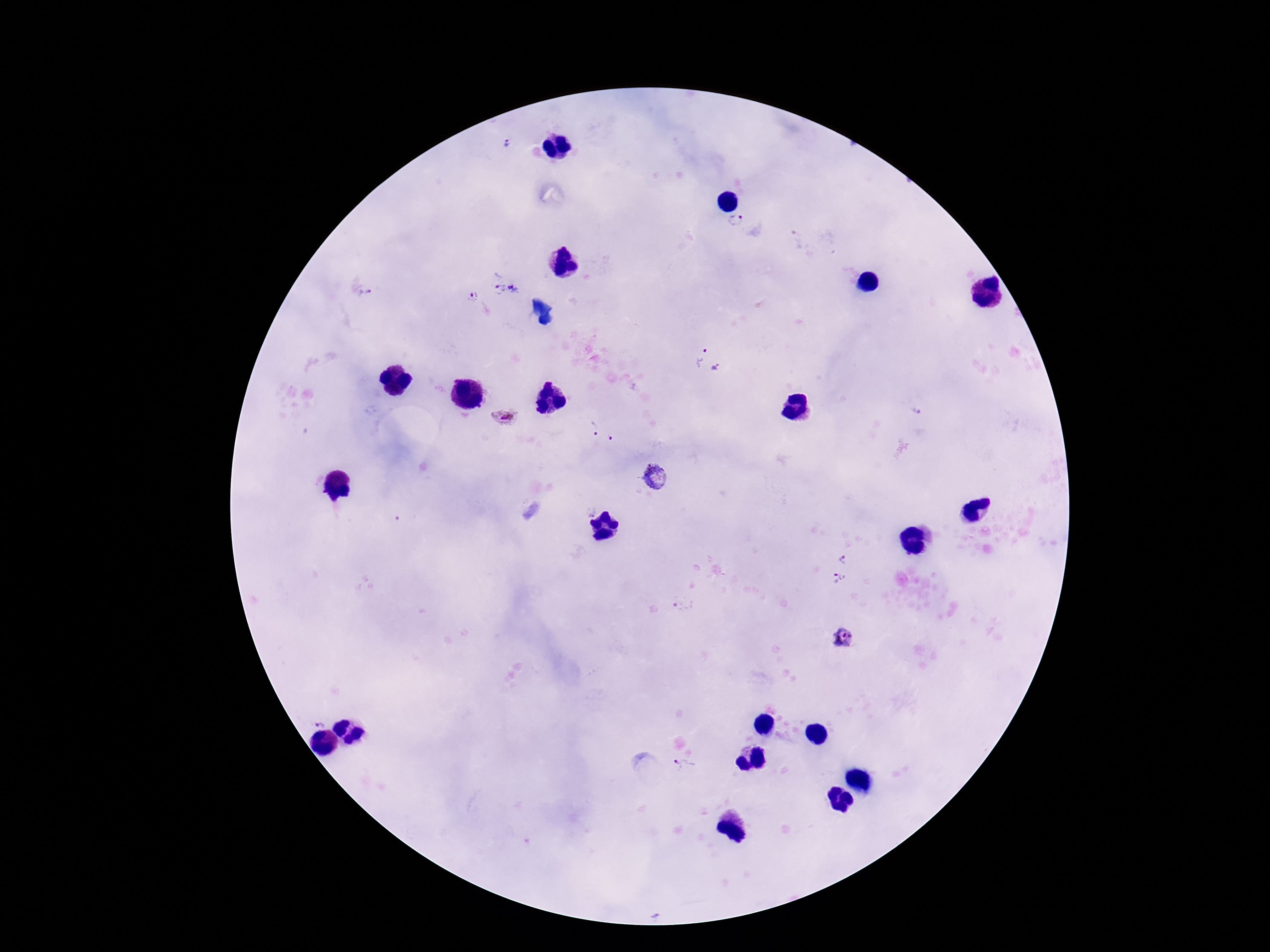
stain = Giemsa
Plasmodium parasite locations = approximate centers as (x, y) in pixels: (506, 144), (735, 220), (506, 286), (363, 291), (473, 296), (709, 361), (917, 412), (505, 418), (591, 430), (609, 439), (655, 478), (844, 557), (839, 578), (682, 605), (844, 637), (319, 721), (684, 766)
magnification = 100x
image size = 1270×952 pixels
patient malaria status = positive
capture = smartphone camera through the microscope eyepiece
preparation = thick peripheral-blood smear
field of view = single